Report the malaria status of this cell.
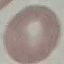

It is uninfected.

preparation = thin smear
capture = smartphone through the microscope eyepiece
stain = Giemsa
image type = cell patch, automatically extracted from a larger field of view and resized to 64 × 64 pixels